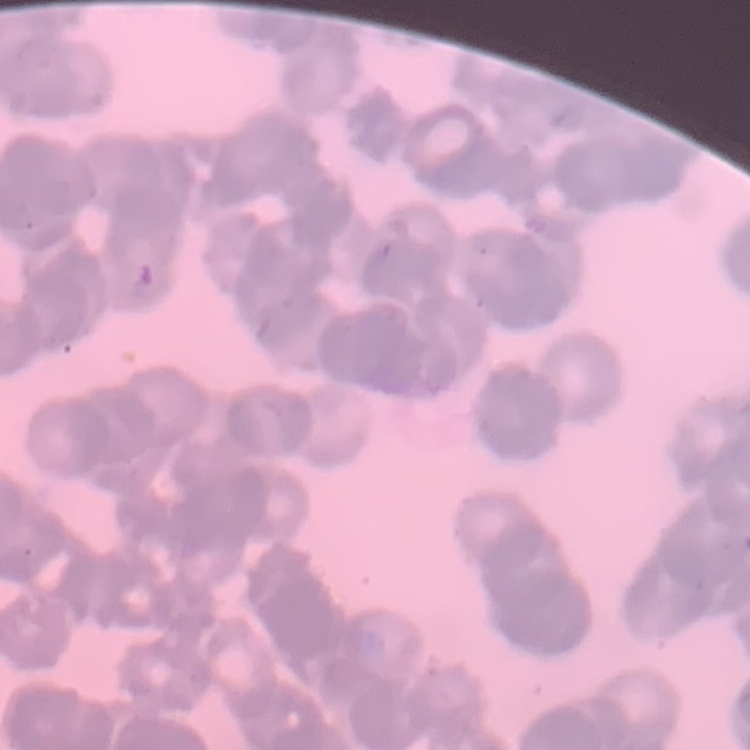 The erythrocytes show rouleaux formation. Thin blood film. One tile cut from a larger photomicrograph. Stained with either Field's or Giemsa.